Classify this cell by malaria status.
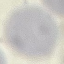
It is uninfected.

Summary:
  - Stain: Giemsa
  - Image type: cell patch, automatically extracted from a larger field of view and resized to 64 × 64 pixels
  - Capture: smartphone through the microscope eyepiece
  - Preparation: thin smear